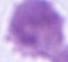
modality = micrograph
identification = red blood cell
magnification = 1000x